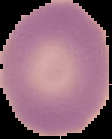

{
  "malaria_status": "uninfected",
  "image_type": "segmented cell region with the area outside set to black",
  "image_size": "112×139 pixels",
  "preparation": "thin blood film"
}